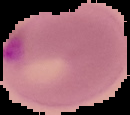
Summary:
  - Malaria status: parasitized
  - Image type: segmented cell region on a black background
  - Image size: 130×115 pixels
  - Preparation: thin blood smear